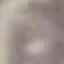
{
  "malaria_status": "uninfected",
  "stain": "Giemsa",
  "image_type": "automatically extracted cell patch, resized to 64 × 64 pixels",
  "capture": "smartphone camera at the microscope eyepiece",
  "preparation": "thin smear"
}